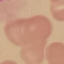
Summary:
  - Result: no malaria parasites seen
  - Preparation: thin blood film
  - Image type: cell patch, automatically extracted from a larger field of view and resized to 64 × 64 pixels
  - Stain: Giemsa
  - Capture: smartphone camera at the microscope eyepiece